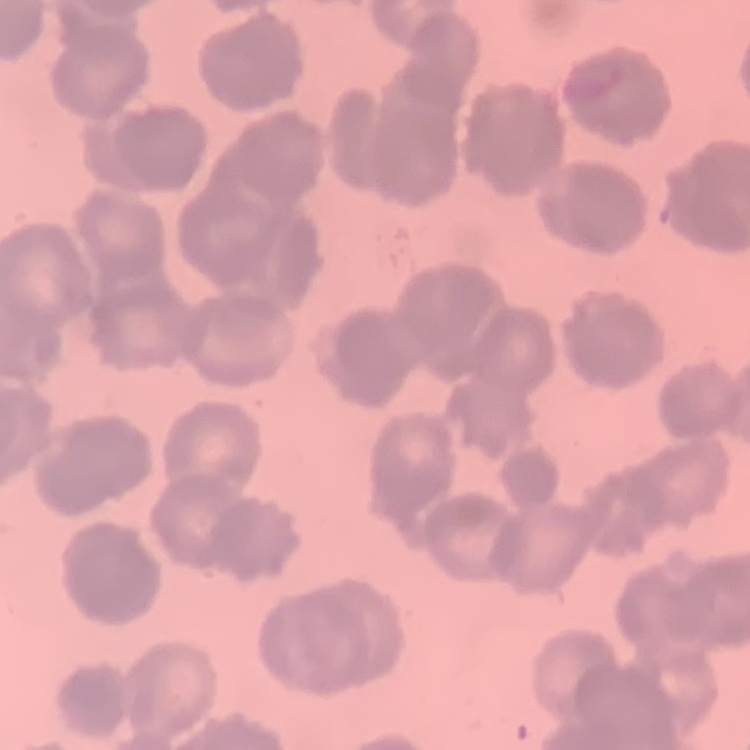 The erythrocytes exhibit rouleaux formation. Thin blood film. One tile cut from a larger photomicrograph. Stained with either Field's or Giemsa.